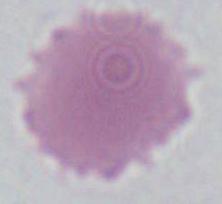
Captured at 1000x magnification. A red blood cell is shown. Photomicrograph.